State which parasite is depicted.
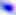
Toxoplasma gondii.

Summary:
  - Modality: micrograph
  - Magnification: 400x